Classify this cell by malaria status.
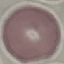

It is uninfected.

Automatically extracted cell patch, resized to 64 × 64 pixels. Giemsa-stained preparation. Thin blood film. Acquired by smartphone through the microscope eyepiece.